Assess this cell for malaria.
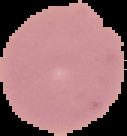
Uninfected.

Image is 127×136 pixels. From a thin blood smear. Cell region segmented out of the field of view; the surrounding area is masked to black.